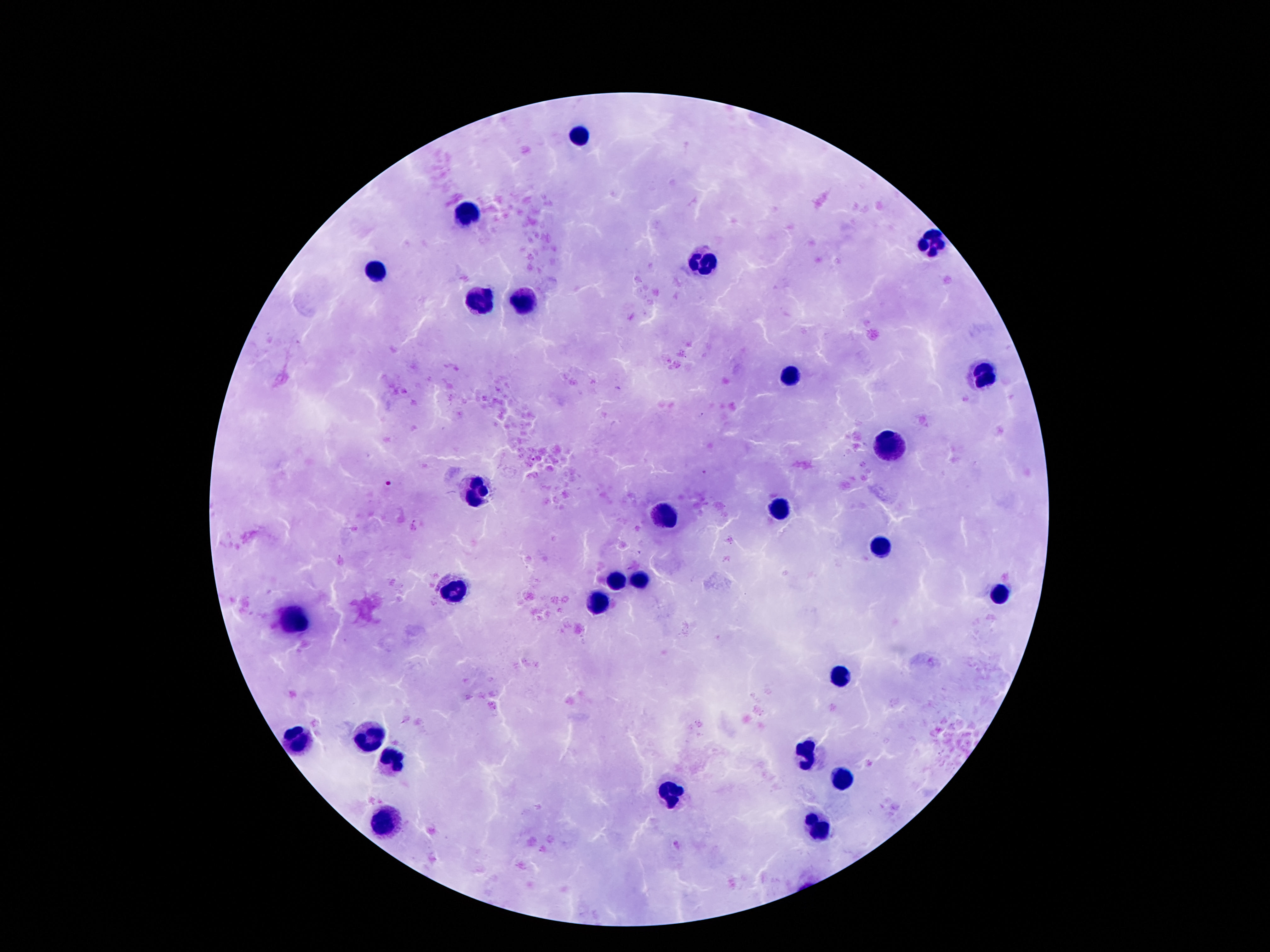
Approximate centers as {x, y} in pixels.
Summary:
  - Leukocyte locations: {578, 134}, {470, 215}, {930, 246}, {702, 259}, {376, 271}, {526, 299}, {476, 307}, {792, 375}, {982, 376}, {892, 444}, {482, 492}, {778, 508}, {664, 514}, {880, 548}, {616, 580}, {638, 580}, {452, 588}, {1000, 594}, {598, 600}, {294, 623}, {838, 674}, {370, 734}, {294, 738}, {806, 756}, {390, 759}, {840, 779}, {668, 794}, {388, 825}, {820, 828}
  - Image size: 1270×952 pixels
  - Patient malaria status: negative
  - Magnification: 100x
  - Capture: smartphone camera through the microscope eyepiece
  - Preparation: thick peripheral-blood smear
  - Field of view: one from this slide
  - Stain: Giemsa